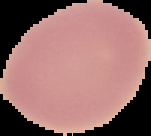

Image is 151×136 pixels. Result: no malaria parasites seen. The area outside the segmented cell region is set to black. From a thin blood smear.